Assess this cell for malaria.
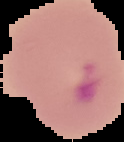
Parasitized.

preparation = thin blood film
image type = segmented cell region on a black background
image size = 124×142 pixels